Classify this cell by malaria status.
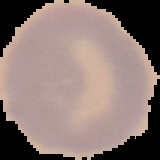

It is uninfected.

Image is 160×160 pixels. Cell region segmented out of the field of view; the surrounding area is masked to black. From a thin blood film.